Name the parasite shown.
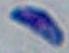
This is Toxoplasma gondii.

Summary:
  - Modality: photomicrograph
  - Magnification: 1000x